Locate every Plasmodium parasite and every leukocyte.
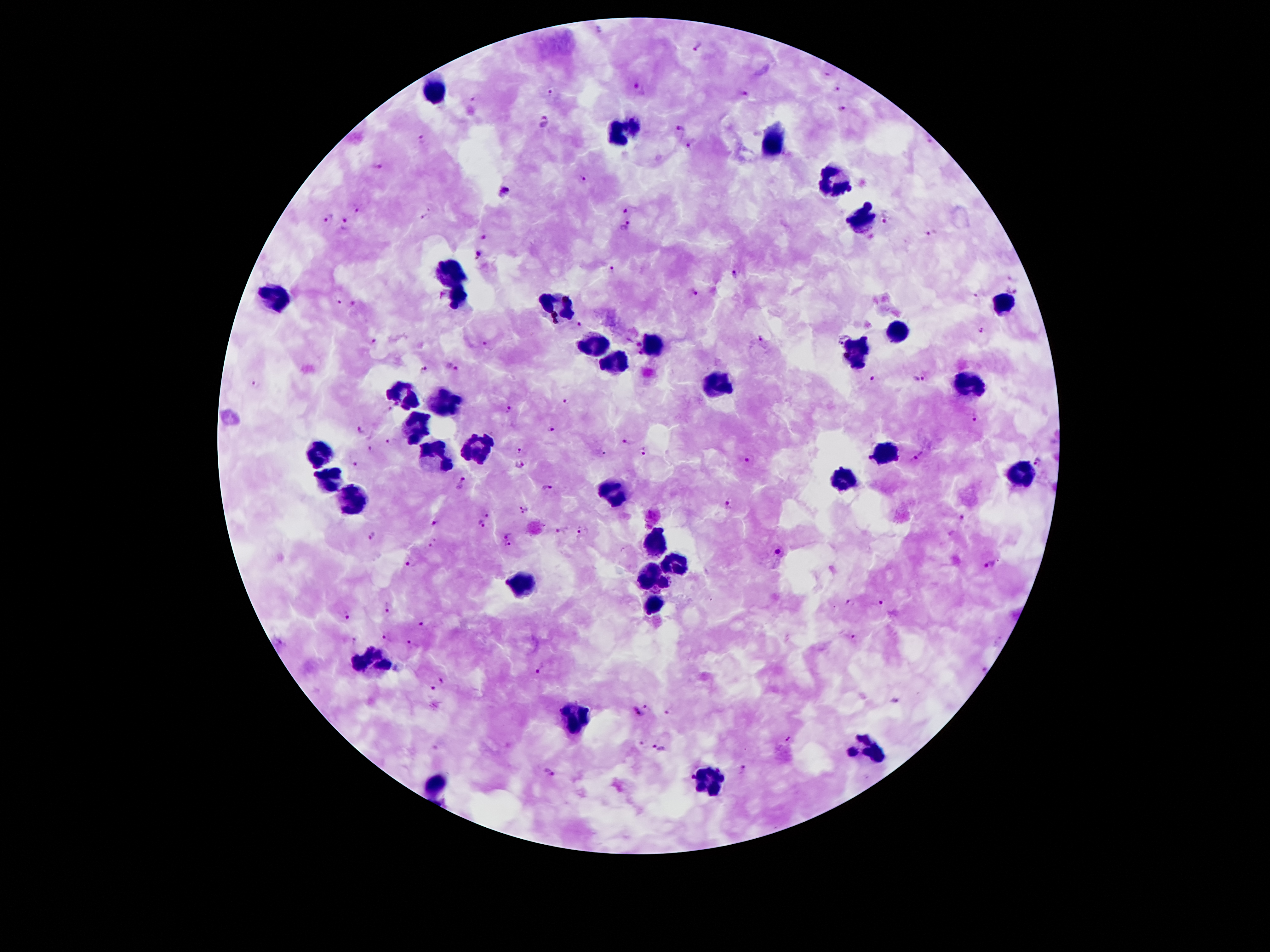

Approximate centers as [x, y] in pixels.
Plasmodium parasites: [596, 29], [697, 47], [826, 73], [641, 89], [839, 89], [550, 91], [743, 93], [473, 96], [840, 108], [545, 119], [680, 129], [423, 138], [928, 140], [690, 143], [382, 167], [583, 177], [507, 192], [357, 207], [626, 210], [425, 216], [328, 218], [886, 219], [347, 222], [625, 224], [933, 232], [484, 236], [478, 253], [610, 268], [736, 276], [1013, 279], [694, 291], [1011, 291], [978, 294], [339, 299], [353, 303], [580, 324], [980, 329], [761, 340], [374, 341], [485, 343], [638, 344], [640, 353], [452, 366], [425, 372], [920, 377], [871, 378], [258, 382], [568, 403], [396, 404], [390, 410], [509, 410], [975, 418], [360, 428], [551, 428], [388, 440], [630, 444], [370, 448], [520, 449], [645, 451], [918, 457], [750, 460], [1037, 460], [520, 463], [357, 464], [463, 481], [547, 487], [727, 504], [524, 508], [487, 514], [962, 518], [434, 521], [482, 522], [561, 529], [579, 531], [371, 534], [508, 534], [435, 544], [508, 544], [777, 550], [410, 562], [989, 565], [881, 602], [850, 604], [390, 607], [346, 615], [425, 623], [852, 637], [387, 639], [355, 641], [411, 643], [543, 669], [984, 669], [447, 682], [431, 690], [894, 700], [649, 707], [670, 712], [635, 714], [791, 740], [641, 742], [658, 748], [743, 771], [549, 772].
Leukocytes: [442, 91], [625, 132], [771, 145], [832, 183], [862, 221], [450, 270], [276, 296], [457, 301], [559, 306], [1000, 306], [898, 331], [653, 342], [594, 347], [855, 354], [615, 362], [712, 384], [967, 385], [402, 389], [445, 402], [416, 425], [475, 448], [889, 451], [324, 453], [435, 463], [1023, 474], [845, 480], [328, 484], [355, 499], [616, 503], [651, 539], [677, 568], [647, 579], [521, 585], [651, 606], [374, 659], [577, 718], [871, 751], [435, 784], [715, 785].

capture: smartphone through the microscope eyepiece
magnification: 100x
stain: Giemsa
field_of_view: one from this slide
patient_malaria_status: infected with Plasmodium falciparum
image_size: 1270×952 pixels
preparation: thick blood smear